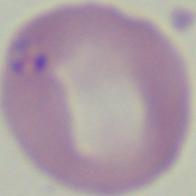
1000x magnification. Micrograph. A Babesia parasite is seen.